Locate and identify every blood parasite.
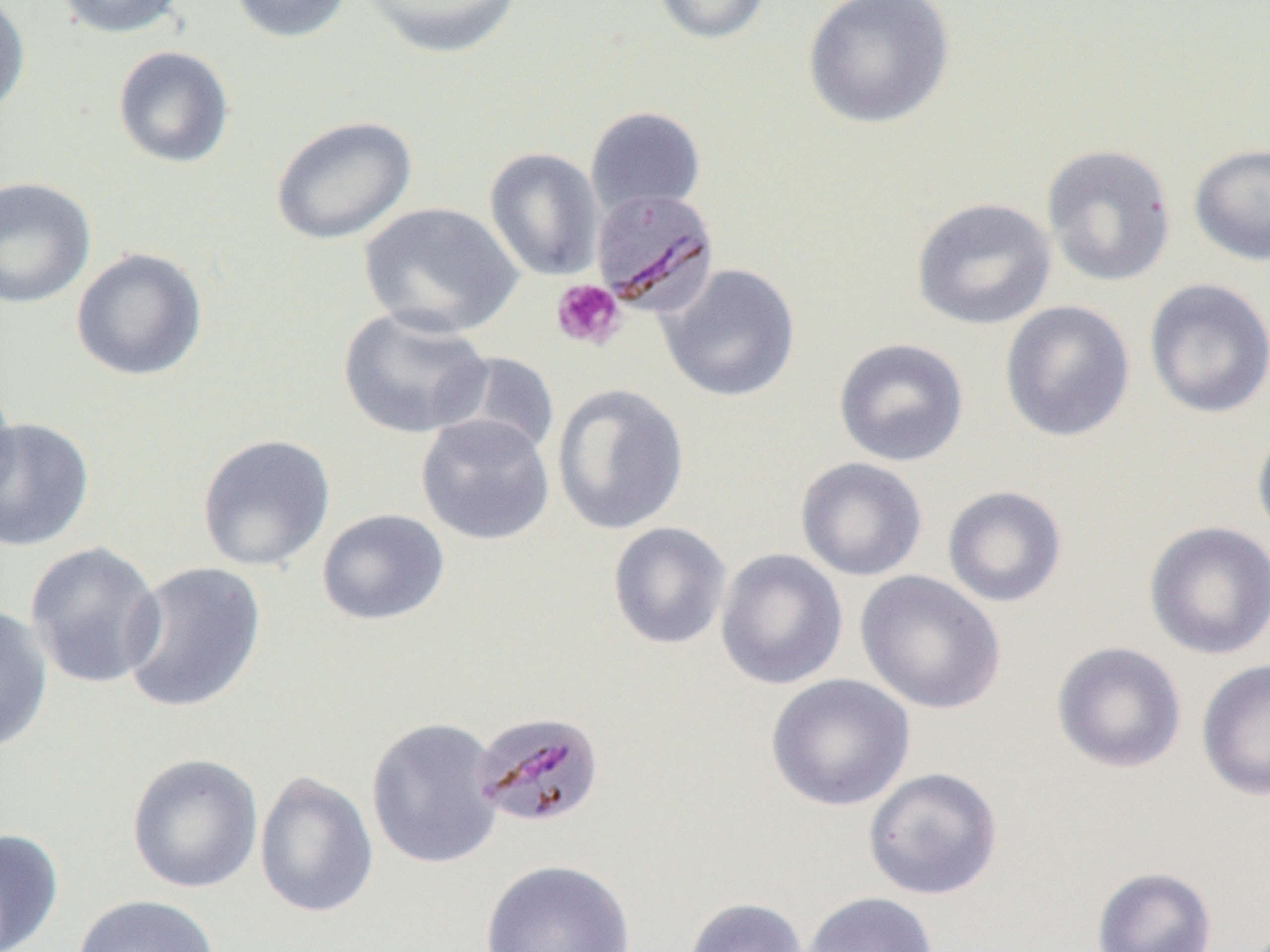
Approximate bounding boxes as named x1/y1/x2/y2 corners in pixels.
Plasmodium malariae-infected red blood cells: (x1=591, y1=188, x2=719, y2=317), (x1=471, y1=711, x2=606, y2=831).
No Plasmodium falciparum, Plasmodium ovale, Plasmodium vivax, Babesia divergens, or Trypanosoma brucei observed.

slide_level_diagnosis: Plasmodium malariae
modality: optical microscopy
image_size: 1270×952 pixels
field_of_view: one of a larger specimen
platelet_locations: 'approximate bounding boxes as named x1/y1/x2/y2 corners in pixels: (x1=550, y1=279, x2=625, y2=351)'
uninfected_red_blood_cell_locations: 'approximate bounding boxes as named x1/y1/x2/y2 corners in pixels: (x1=54, y1=0, x2=188, y2=39), (x1=227, y1=0, x2=355, y2=44), (x1=360, y1=0, x2=524, y2=59), (x1=650, y1=0, x2=774, y2=45), (x1=802, y1=0, x2=955, y2=129), (x1=0, y1=1, x2=31, y2=118), (x1=112, y1=45, x2=235, y2=169), (x1=585, y1=106, x2=706, y2=218), (x1=270, y1=115, x2=417, y2=245), (x1=1041, y1=143, x2=1177, y2=287), (x1=1189, y1=143, x2=1270, y2=266), (x1=484, y1=148, x2=603, y2=281), (x1=0, y1=177, x2=96, y2=308), (x1=911, y1=197, x2=1057, y2=330), (x1=359, y1=202, x2=523, y2=339), (x1=70, y1=247, x2=208, y2=382), (x1=658, y1=262, x2=801, y2=403), (x1=1143, y1=277, x2=1270, y2=419), (x1=1000, y1=300, x2=1135, y2=442), (x1=337, y1=306, x2=493, y2=439), (x1=833, y1=337, x2=969, y2=467), (x1=440, y1=351, x2=560, y2=461), (x1=0, y1=379, x2=20, y2=507), (x1=551, y1=383, x2=690, y2=536), (x1=415, y1=414, x2=555, y2=545), (x1=0, y1=417, x2=95, y2=552), (x1=1252, y1=418, x2=1270, y2=547), (x1=196, y1=433, x2=336, y2=572), (x1=795, y1=457, x2=927, y2=581), (x1=943, y1=486, x2=1067, y2=607), (x1=317, y1=509, x2=450, y2=626), (x1=607, y1=521, x2=732, y2=650), (x1=1144, y1=521, x2=1270, y2=661), (x1=23, y1=541, x2=166, y2=689), (x1=715, y1=548, x2=848, y2=690), (x1=120, y1=561, x2=267, y2=714), (x1=855, y1=570, x2=1006, y2=714), (x1=0, y1=604, x2=54, y2=754), (x1=1051, y1=641, x2=1187, y2=773), (x1=1196, y1=658, x2=1270, y2=802), (x1=765, y1=673, x2=915, y2=811), (x1=365, y1=717, x2=504, y2=870), (x1=126, y1=752, x2=263, y2=894), (x1=862, y1=767, x2=1003, y2=901), (x1=253, y1=770, x2=379, y2=919), (x1=0, y1=827, x2=65, y2=951), (x1=480, y1=858, x2=636, y2=952), (x1=1091, y1=866, x2=1218, y2=952), (x1=800, y1=891, x2=939, y2=952), (x1=71, y1=893, x2=221, y2=952), (x1=684, y1=897, x2=808, y2=952)'
magnification: 1000x
preparation: thin blood smear